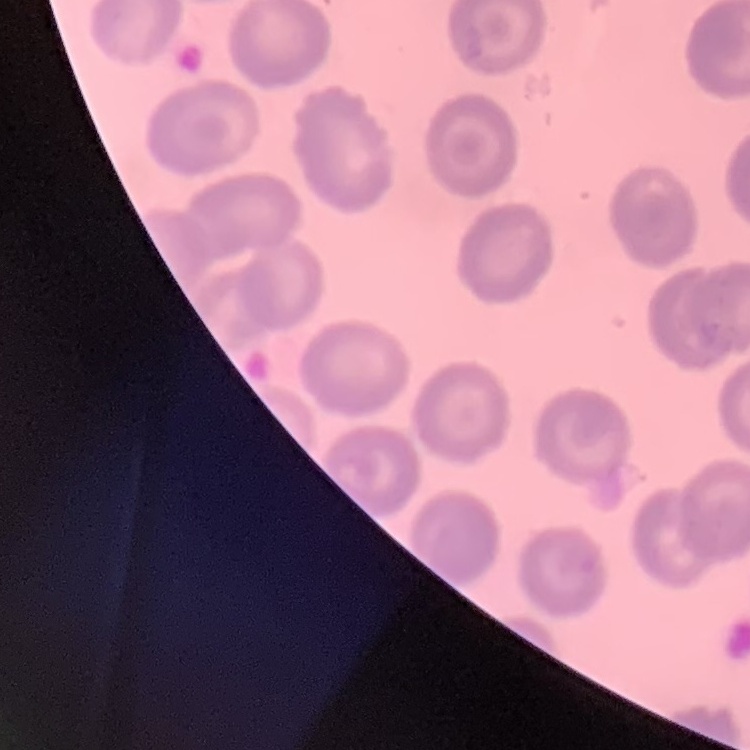

The erythrocytes show no rouleaux formation. Thin blood film. Stained with either Field's or Giemsa. One tile cut from a larger photomicrograph.